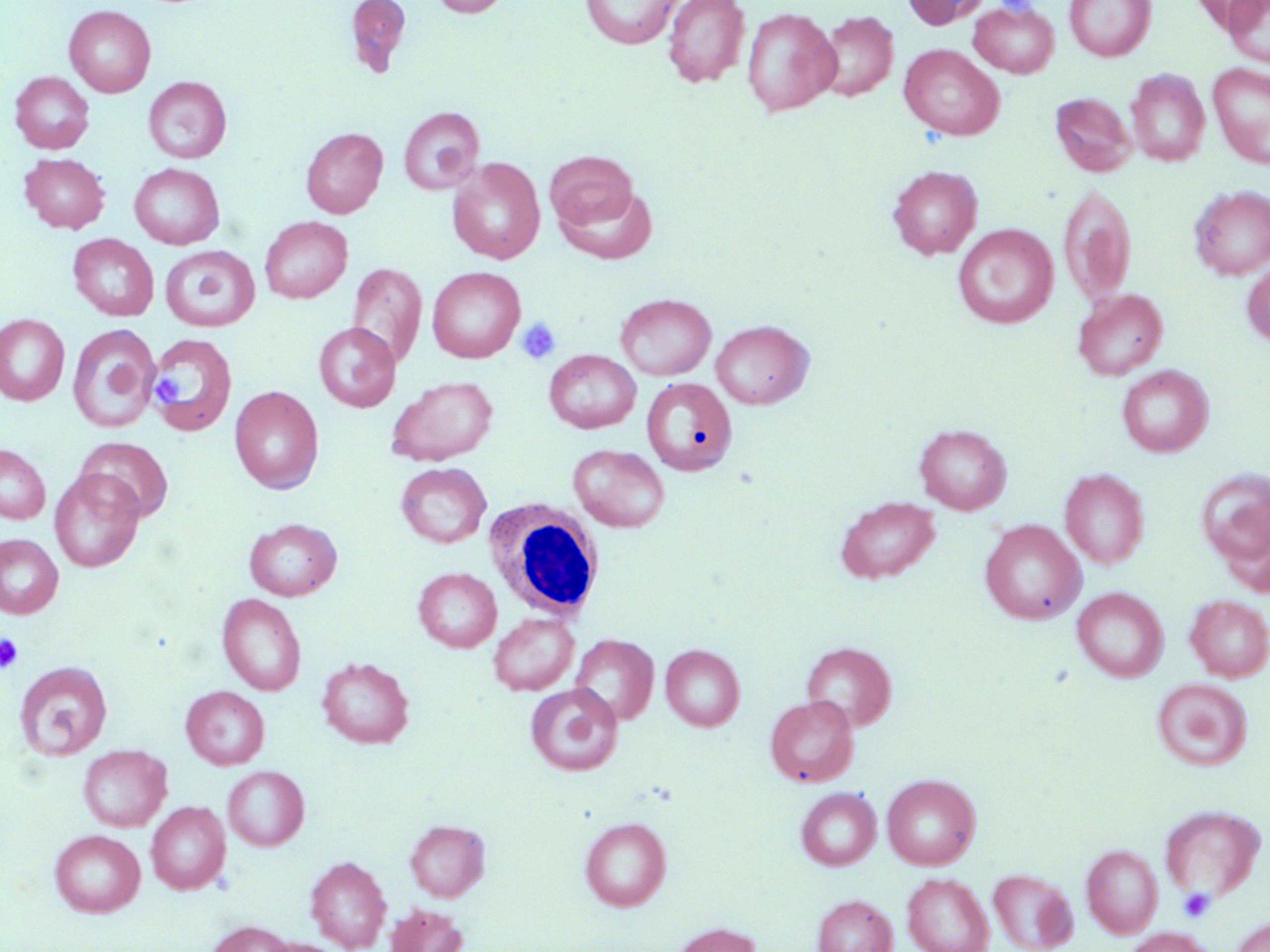
Approximate bounding boxes as (x1, y1, x2, y2) in pixels. Uninfected red blood cell locations: (345, 0, 412, 78), (430, 0, 512, 18), (580, 0, 684, 49), (662, 0, 751, 88), (902, 0, 990, 29), (1065, 0, 1156, 61), (969, 1, 1060, 78), (1224, 1, 1270, 69), (64, 5, 156, 97), (741, 6, 841, 117), (815, 11, 898, 101), (899, 44, 1004, 141), (1207, 62, 1270, 168), (1126, 69, 1209, 166), (10, 71, 94, 154), (143, 76, 231, 163), (1050, 92, 1136, 177), (398, 106, 485, 195), (301, 127, 387, 218), (544, 150, 639, 231), (20, 153, 110, 233), (447, 157, 545, 265), (129, 163, 224, 249), (888, 165, 982, 259), (1058, 184, 1136, 305), (555, 185, 658, 264), (1189, 186, 1270, 279), (259, 216, 353, 303), (953, 224, 1058, 328), (69, 233, 158, 320), (160, 245, 260, 332), (1242, 260, 1270, 347), (347, 262, 427, 367), (427, 266, 525, 362), (1073, 288, 1168, 380), (615, 293, 716, 380), (0, 314, 70, 406), (711, 320, 814, 409), (67, 323, 161, 432), (313, 323, 400, 411), (146, 332, 238, 436), (544, 350, 641, 433), (1117, 365, 1213, 457), (387, 376, 498, 466), (641, 377, 737, 475), (229, 386, 324, 493), (914, 424, 1012, 514), (76, 436, 174, 522), (0, 443, 51, 524), (569, 444, 669, 532), (395, 462, 490, 548), (1196, 467, 1270, 577), (50, 469, 144, 573), (1060, 469, 1150, 569), (834, 496, 940, 584), (244, 518, 342, 601), (980, 520, 1086, 624), (0, 534, 64, 619), (413, 568, 501, 652), (1072, 587, 1168, 682), (217, 594, 306, 696), (1185, 594, 1270, 682), (488, 612, 579, 695), (570, 634, 659, 725), (801, 642, 896, 730), (661, 644, 745, 731), (317, 656, 414, 748), (14, 661, 113, 760), (1152, 678, 1252, 770), (525, 683, 622, 776), (181, 685, 270, 769), (765, 694, 859, 787), (78, 745, 172, 832), (223, 765, 309, 850), (882, 773, 980, 869), (796, 787, 881, 870), (146, 802, 230, 894), (1159, 804, 1265, 901), (580, 816, 671, 910), (405, 819, 490, 901), (49, 829, 145, 917), (1081, 844, 1162, 938), (306, 855, 391, 952), (988, 869, 1077, 952), (902, 872, 994, 952), (812, 894, 897, 952), (385, 903, 469, 952), (1231, 916, 1270, 952), (205, 920, 294, 952), (670, 923, 763, 952), (1124, 927, 1215, 952). White blood cell locations: (484, 499, 605, 621). Platelet locations: (515, 317, 561, 365), (151, 368, 186, 410), (0, 634, 23, 673), (1178, 888, 1215, 922). Slide-level diagnosis: no evidence of blood parasites. May-Grünwald-Giemsa-stained preparation. Thin blood smear. Captured at 1000x magnification. Image is 1270×952 pixels. One field of a larger specimen. Optical microscopy.